Assess the morphology of the red blood cells.
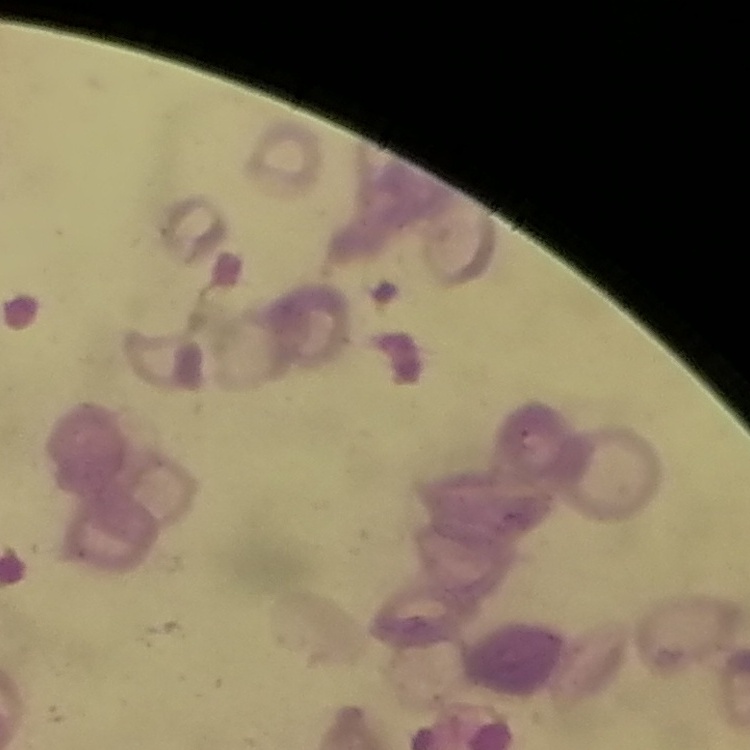

Rouleaux formation.

preparation = thin peripheral smear
stain = Field's or Giemsa
image type = square crop of a larger photomicrograph